Assess this cell for malaria.
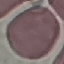

It is uninfected.

Summary:
  - Image type: cell patch, automatically extracted from a larger field of view and resized to 64 × 64 pixels
  - Preparation: thin blood film
  - Capture: smartphone through the microscope eyepiece
  - Stain: Giemsa